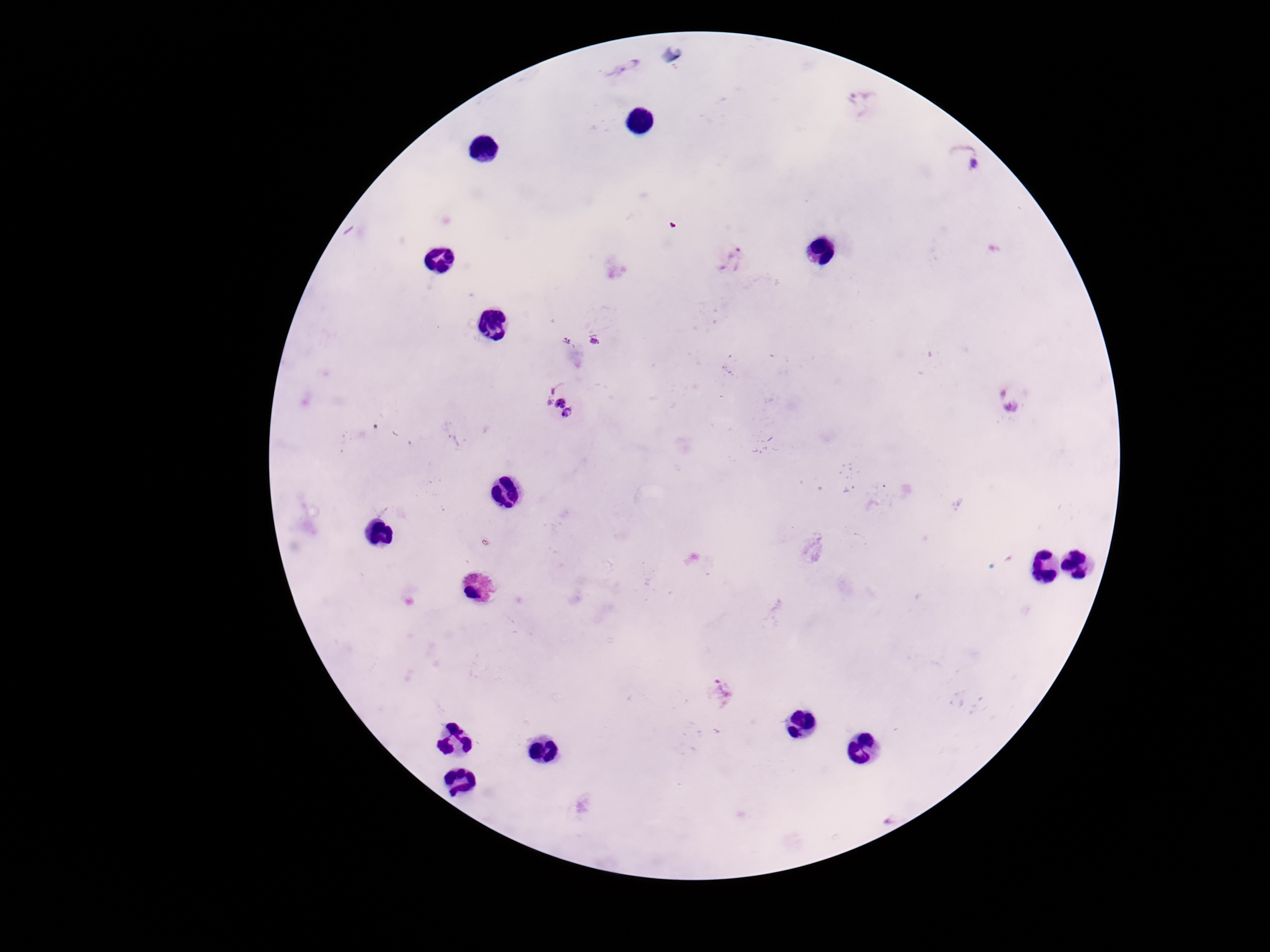

Approximate object centers, in pixels from the top-left corner. Plasmodium parasite locations: (x=625, y=66), (x=864, y=104), (x=963, y=156), (x=731, y=260), (x=594, y=342), (x=1009, y=400), (x=559, y=404), (x=722, y=695). Patient malaria status: infected. Smartphone photograph taken through the microscope eyepiece. Image is 1270×952 pixels. 100x magnification. Thick blood film. Single field of view. Giemsa stain.